Describe the morphology of the red blood cells.
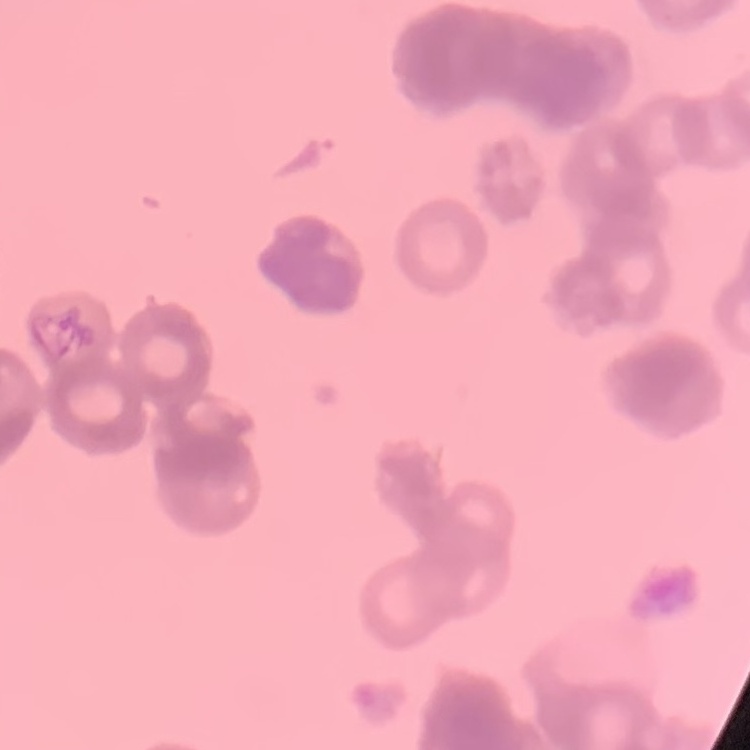

They show rouleaux formation.

preparation = thin blood smear
stain = Field's or Giemsa
image type = square crop of a larger photomicrograph